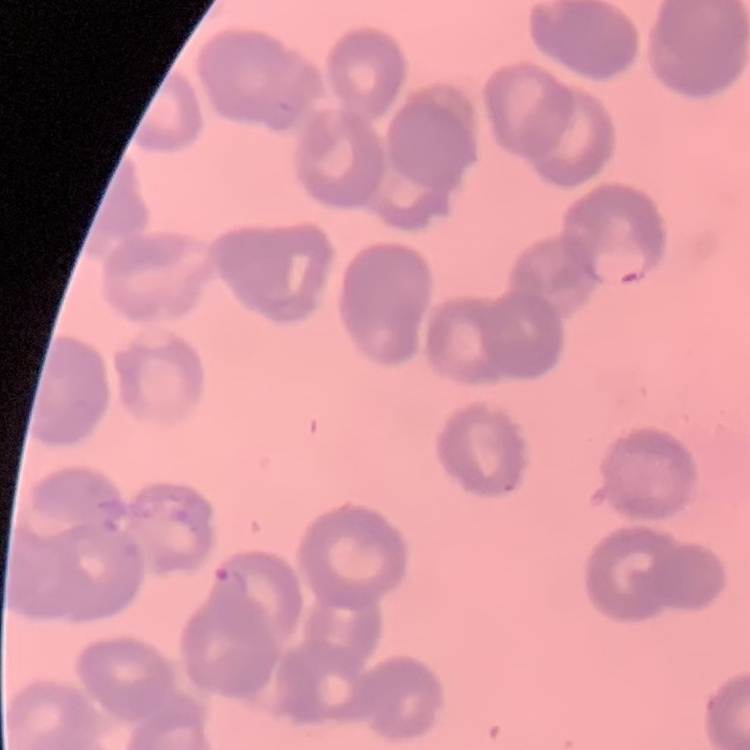

The red blood cells exhibit rouleaux formation. Stained with either Field's or Giemsa. Square crop of a larger photomicrograph. Thin peripheral smear.